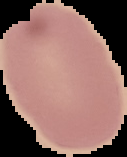

From a thin blood smear. Image is 127×157 pixels. Malaria status: uninfected. Segmented cell region on a black background.